Locate every P. falciparum parasite and give its life-cycle stage, and locate every leukocyte and any debris.
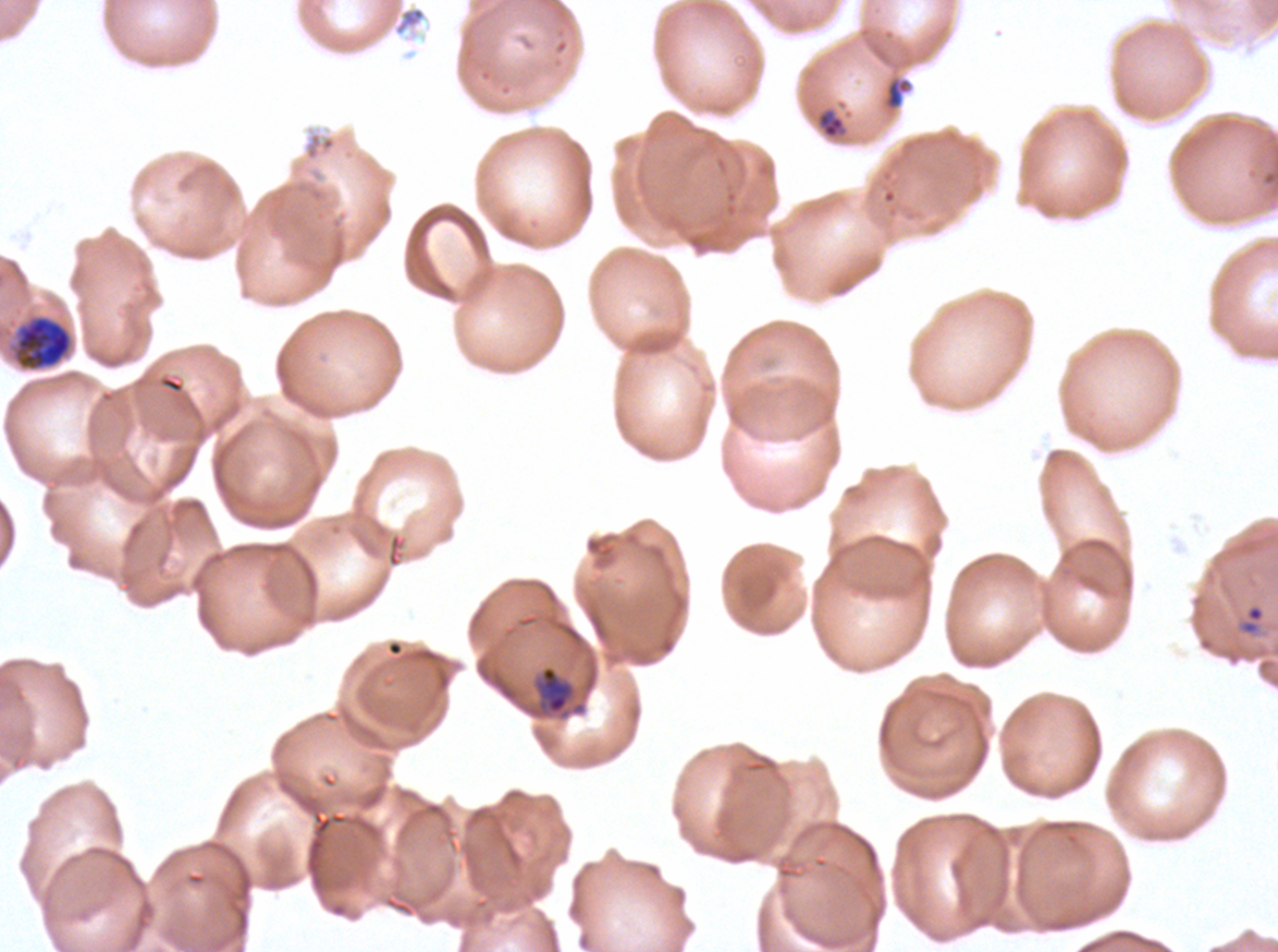
Approximate bounding rectangles given as corner coordinates in pixels from the top-left.
Rings: (x1=1238, y1=604, x2=1266, y2=636).
Late-ring/early-trophozoite forms: (x1=817, y1=107, x2=846, y2=140), (x1=540, y1=665, x2=572, y2=714).
Early schizonts: (x1=16, y1=315, x2=72, y2=370).
No mid trophozoites, late trophozoites, late schizonts, segmenters, gametocytes, leukocytes, or debris observed.

preparation = thin blood smear
stain = Giemsa
image size = 1278×952 pixels
field of view = sub-image separated from a larger composite
specimen = ex-vivo P. falciparum culture from a patient in The Gambia, grown for 24 to 48 hours
life-cycle stages observed = ring, late-ring/early-trophozoite, early schizont